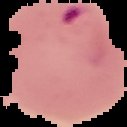

Summary:
  - Image type: segmented cell region on a black background
  - Image size: 127×127 pixels
  - Result: Plasmodium parasites identified
  - Preparation: thin blood smear